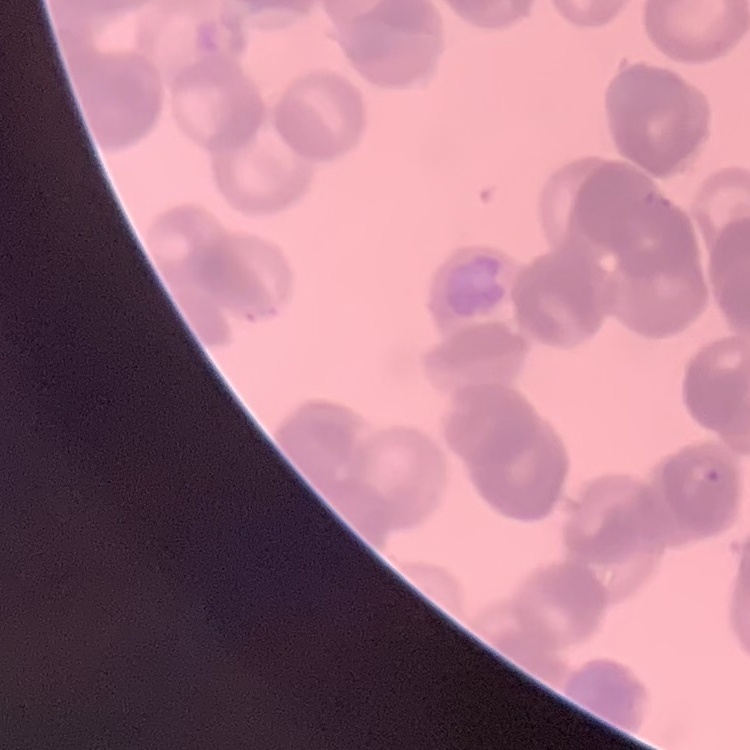
red blood cell morphology = rouleaux formation
stain = Field's or Giemsa
preparation = thin blood film
image type = square crop of a larger photomicrograph